Locate every Plasmodium falciparum-infected red blood cell.
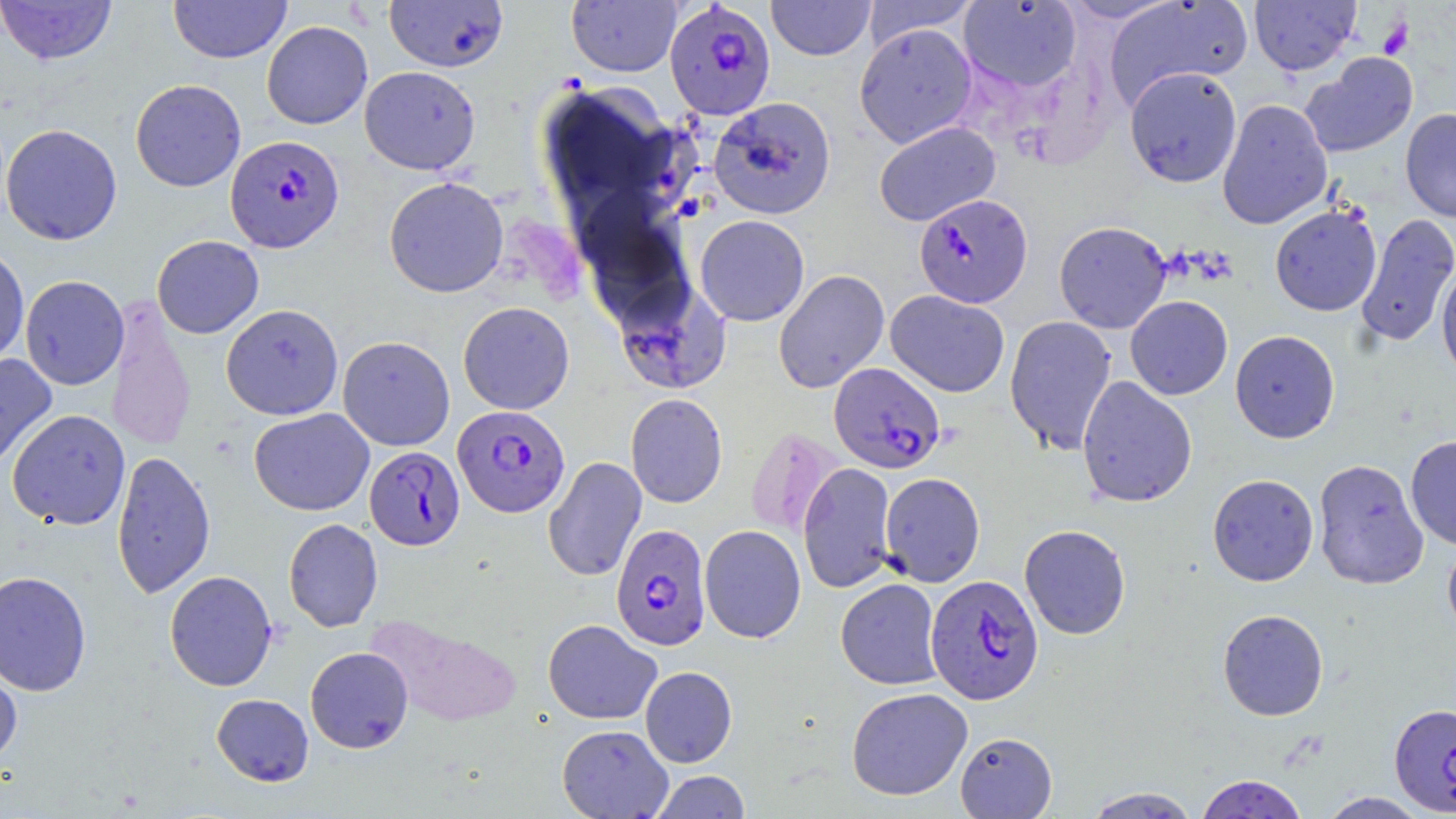
Approximate bounding boxes as (x1,y1)-(x2,y2) corner pairs in pixels.
Plasmodium falciparum-infected red blood cells: (664,2)-(776,120), (225,135)-(344,253), (914,193)-(1033,308), (828,362)-(945,473), (452,405)-(570,518), (364,446)-(465,550), (611,524)-(711,651), (925,574)-(1044,704), (1389,703)-(1456,816).

slide-level diagnosis = Plasmodium falciparum
platelet locations = approximate bounding boxes as (x1,y1)-(x2,y2) corner pairs in pixels: (1378,16)-(1414,59)
preparation = thin blood smear
uninfected red blood cell locations = approximate bounding boxes as (x1,y1)-(x2,y2) corner pairs in pixels: (0,0)-(117,65), (384,0)-(508,73), (766,0)-(876,60), (1059,0)-(1182,23), (1104,0)-(1253,107), (1249,0)-(1361,75), (168,1)-(291,63), (566,1)-(682,77), (861,1)-(980,48), (958,1)-(1082,93), (261,21)-(373,129), (854,23)-(978,149), (1301,52)-(1418,158), (359,66)-(481,174), (1124,66)-(1243,187), (130,79)-(246,192), (708,96)-(837,219), (1217,98)-(1333,230), (1400,108)-(1456,222), (873,121)-(1001,226), (1,124)-(123,245), (384,176)-(508,298), (1270,205)-(1382,316), (1356,213)-(1456,347), (695,215)-(810,326), (1054,220)-(1172,334), (152,235)-(264,339), (0,244)-(29,368), (1436,260)-(1456,383), (773,269)-(889,394), (20,275)-(129,391), (613,278)-(731,395), (886,290)-(1010,397), (1125,296)-(1233,400), (106,297)-(197,455), (458,301)-(574,415), (220,303)-(343,420), (1004,315)-(1117,455), (1230,330)-(1340,444), (338,336)-(455,451), (0,353)-(57,472), (1076,376)-(1197,508), (625,393)-(728,508), (249,408)-(374,515), (7,409)-(130,530), (745,426)-(843,541), (1405,435)-(1456,550), (111,449)-(216,599), (543,456)-(647,582), (1312,458)-(1429,589), (798,462)-(898,593), (879,472)-(985,587), (1207,473)-(1319,586), (283,518)-(383,632), (699,524)-(806,643), (1019,524)-(1131,640), (1442,537)-(1456,643), (0,570)-(92,696), (164,570)-(277,692), (836,578)-(943,689), (1217,608)-(1329,721), (368,613)-(523,728), (543,619)-(662,724), (305,647)-(413,753), (0,660)-(22,769), (640,666)-(737,767), (846,687)-(973,800), (212,693)-(313,786), (556,724)-(672,818), (955,731)-(1057,818), (650,771)-(750,818), (1195,774)-(1308,818), (1082,786)-(1203,818), (1318,792)-(1430,818)
field of view = one of a larger specimen
magnification = 1000x
image size = 1456×819 pixels
modality = optical microscopy
stain = May-Grünwald-Giemsa